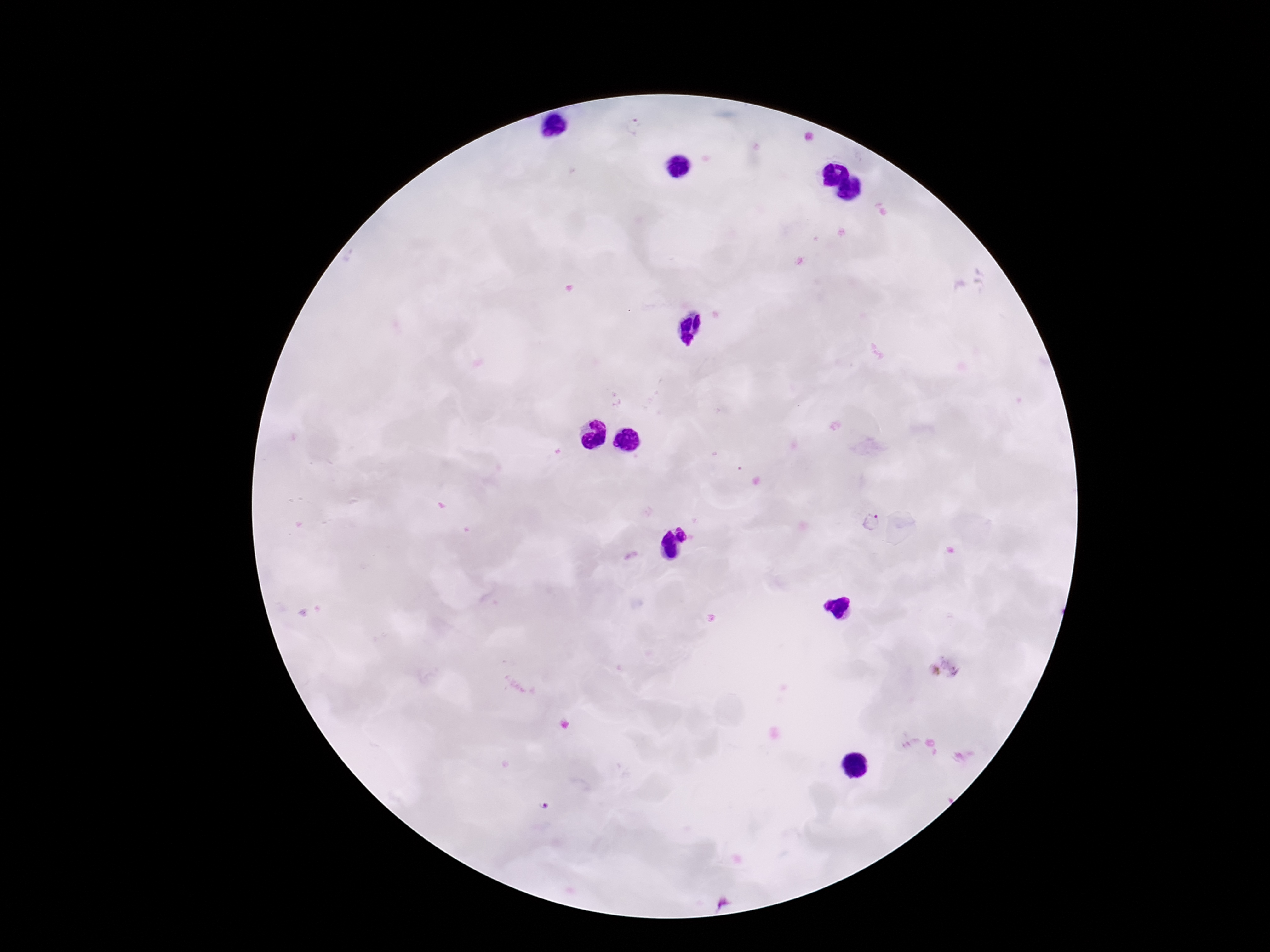

Approximate centers as (x, y) in pixels. Plasmodium parasite locations: (632, 127), (873, 522), (945, 668), (544, 806). Single field of view. Patient malaria status: infected. Image is 1270×952 pixels. Giemsa stain. 100x magnification. Thick peripheral-blood smear. Photographed through the microscope eyepiece with a smartphone camera.